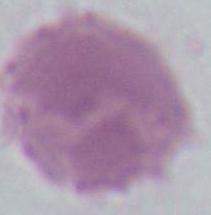 Photomicrograph. 1000x magnification. An erythrocyte is seen.